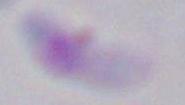
modality = photomicrograph
identification = Toxoplasma gondii
magnification = 1000x